Locate and identify every blood parasite.
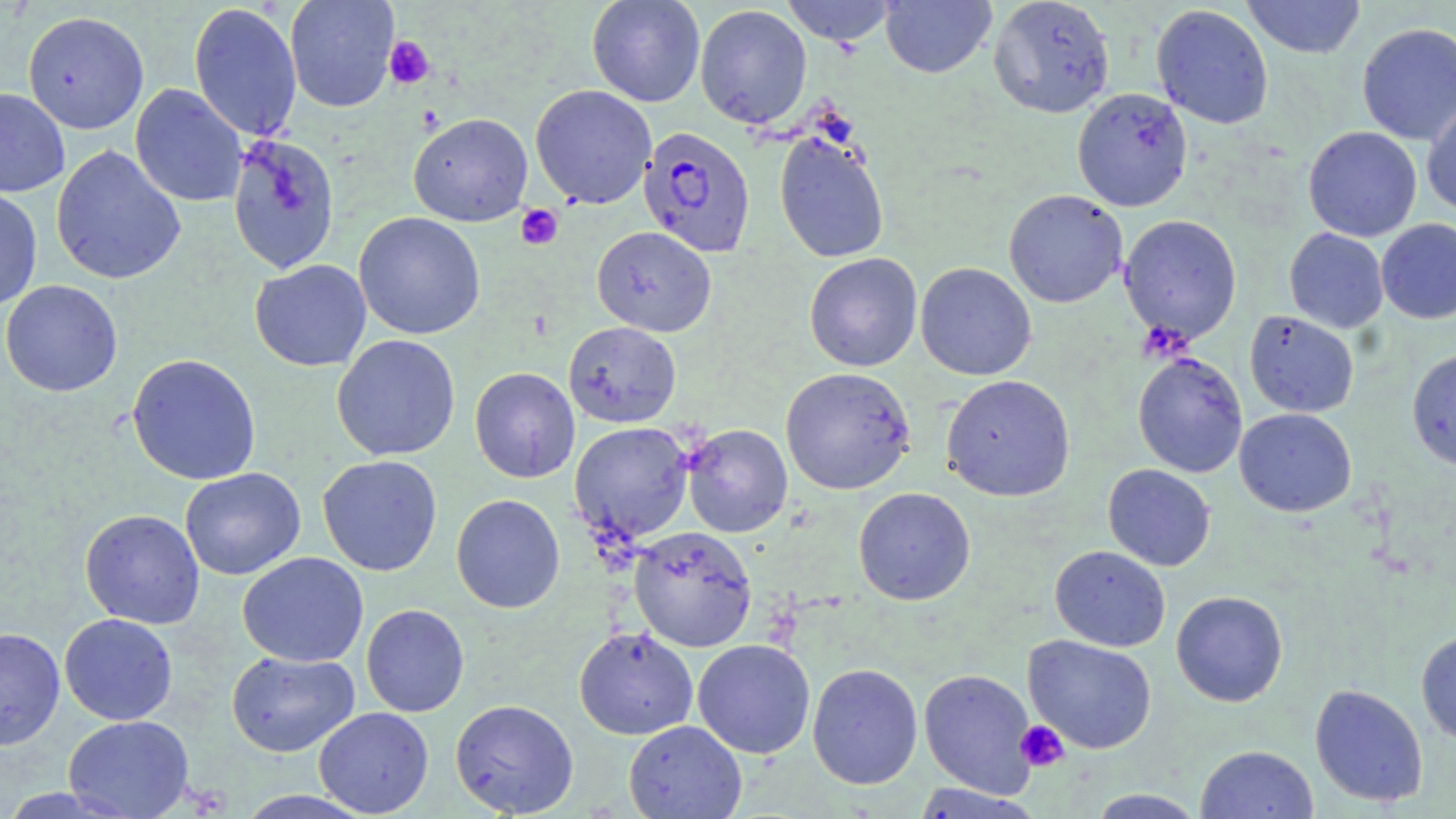
Approximate bounding boxes as [x1, y1, x2, y2] in pixels.
Plasmodium falciparum-infected red blood cells: [639, 125, 755, 257].
No Plasmodium ovale, Plasmodium malariae, Plasmodium vivax, Babesia divergens, or Trypanosoma brucei observed.

Summary:
  - Platelet locations: [383, 36, 435, 90], [515, 204, 563, 251], [1015, 720, 1070, 772]
  - Uninfected red blood cell locations: [284, 0, 399, 112], [586, 0, 706, 107], [780, 0, 897, 46], [881, 0, 996, 78], [988, 0, 1115, 118], [1241, 0, 1366, 59], [189, 2, 302, 141], [695, 4, 812, 129], [1151, 4, 1274, 129], [22, 10, 149, 134], [1357, 23, 1456, 144], [130, 83, 248, 207], [530, 84, 657, 209], [0, 87, 70, 197], [1072, 87, 1193, 212], [1421, 98, 1456, 217], [408, 112, 533, 227], [1303, 126, 1421, 241], [774, 132, 890, 264], [225, 133, 341, 275], [51, 144, 186, 285], [0, 187, 43, 310], [1004, 189, 1128, 308], [354, 212, 485, 340], [1119, 214, 1242, 344], [1376, 218, 1456, 324], [592, 226, 717, 337], [1284, 228, 1388, 333], [804, 252, 923, 371], [250, 259, 371, 371], [915, 262, 1036, 380], [0, 280, 123, 397], [1244, 310, 1359, 417], [563, 321, 681, 428], [332, 334, 460, 461], [1406, 348, 1456, 470], [1133, 352, 1248, 478], [126, 353, 262, 485], [469, 367, 580, 483], [780, 367, 915, 495], [941, 374, 1075, 502], [1234, 408, 1356, 517], [569, 422, 694, 544], [681, 423, 793, 538], [317, 455, 442, 576], [1103, 464, 1215, 571], [180, 467, 306, 580], [853, 487, 976, 605], [451, 494, 565, 613], [79, 509, 205, 629], [629, 526, 757, 651], [1049, 545, 1170, 652], [237, 552, 369, 667], [1171, 590, 1288, 707], [361, 604, 469, 717], [59, 613, 178, 725], [0, 627, 66, 750], [573, 627, 699, 740], [1416, 630, 1456, 744], [1023, 634, 1157, 754], [692, 639, 815, 759], [226, 650, 360, 757], [807, 662, 923, 790], [918, 668, 1038, 798], [1310, 684, 1428, 807], [450, 698, 579, 817], [313, 707, 434, 817], [63, 714, 194, 819], [624, 719, 746, 819], [1195, 745, 1319, 819], [910, 783, 1043, 818], [1088, 788, 1206, 818], [232, 790, 375, 818]
  - Slide-level diagnosis: Plasmodium falciparum
  - Preparation: thin blood film
  - Stain: May-Grünwald-Giemsa
  - Magnification: 1000x
  - Image size: 1456×819 pixels
  - Field of view: single
  - Modality: optical microscopy